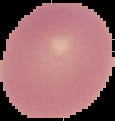
image type = segmented cell region on a black background
malaria status = uninfected
preparation = thin blood film
image size = 115×121 pixels